Assess this cell for malaria.
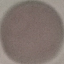
Uninfected.

image type = cell patch, automatically extracted from a larger field of view and resized to 64 × 64 pixels
capture = smartphone camera at the microscope eyepiece
stain = Giemsa
preparation = thin blood smear